Name the blood parasite species.
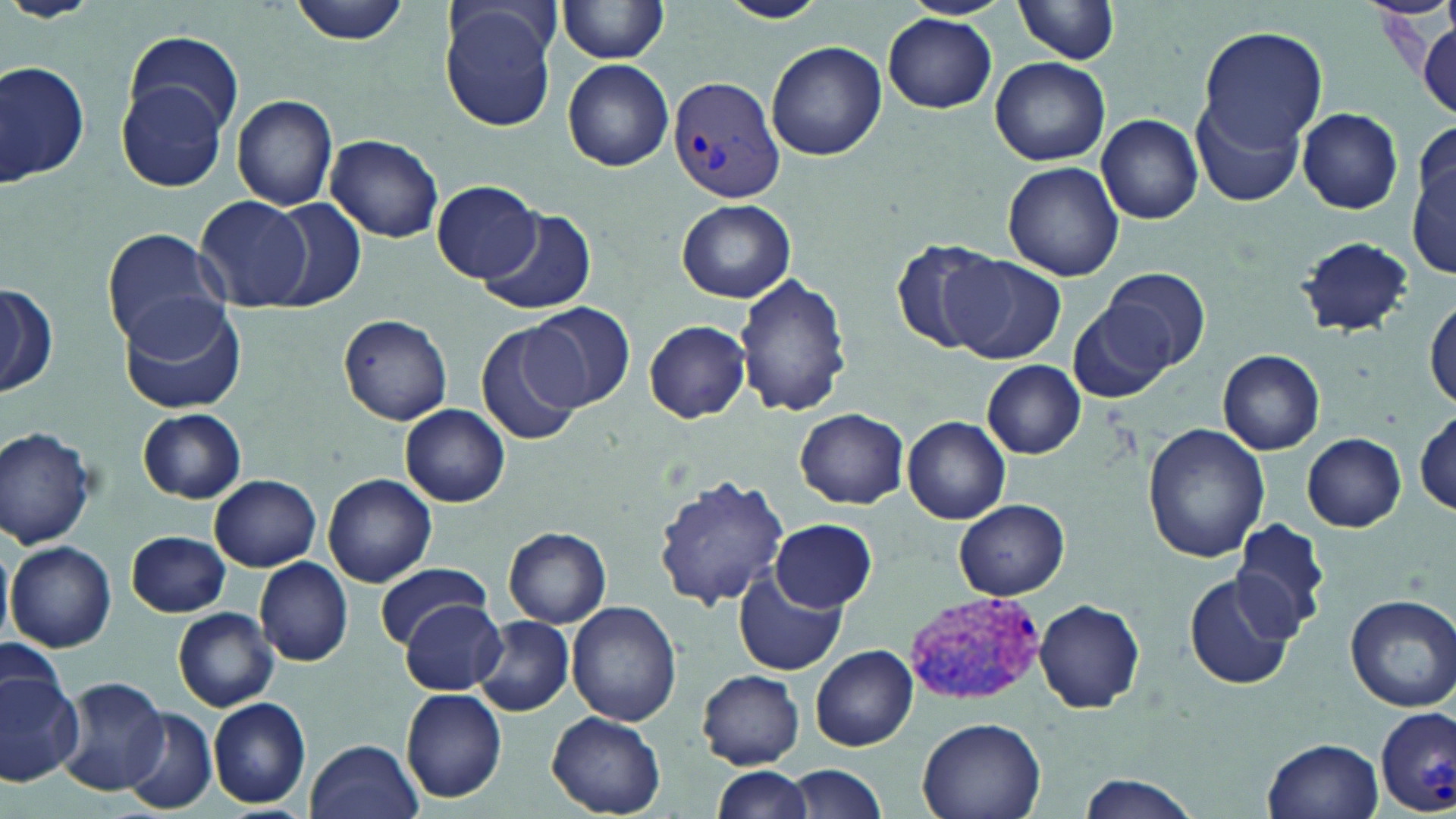

Plasmodium vivax.

magnification: 1000x
stain: May-Grünwald-Giemsa
field_of_view: one of a larger specimen
preparation: thin blood film
plasmodium_vivax_infected_red_blood_cell_locations: 'approximate bounding boxes as (x1,y1)-(x2,y2) corner pairs in pixels: (666,74)-(786,206), (901,593)-(1045,704), (1376,706)-(1456,812)'
image_size: 1456×819 pixels
modality: optical microscopy
uninfected_red_blood_cell_locations: 'approximate bounding boxes as (x1,y1)-(x2,y2) corner pairs in pixels: (288,0)-(412,44), (718,0)-(828,24), (1017,1)-(1120,64), (556,2)-(670,63), (438,3)-(559,133), (883,13)-(997,112), (1414,23)-(1455,120), (1199,27)-(1328,150), (123,32)-(245,137), (766,41)-(886,161), (991,57)-(1110,165), (1,58)-(90,188), (562,60)-(674,172), (117,81)-(227,193), (230,94)-(338,210), (1194,98)-(1305,208), (1296,108)-(1404,214), (1097,113)-(1203,224), (325,135)-(445,243), (1411,148)-(1454,277), (1002,161)-(1125,281), (432,180)-(545,283), (194,196)-(313,312), (263,198)-(365,308), (677,199)-(796,304), (478,210)-(597,315), (102,227)-(227,352), (1296,235)-(1414,337), (891,237)-(1008,354), (945,254)-(1066,365), (1099,266)-(1214,375), (734,272)-(852,418), (1,283)-(55,399), (119,294)-(250,414), (1427,297)-(1456,408), (1069,298)-(1176,403), (525,301)-(635,411), (337,314)-(454,426), (644,320)-(751,422), (475,321)-(586,447), (1218,350)-(1323,454), (983,361)-(1086,458), (398,403)-(512,507), (136,408)-(247,503), (794,408)-(908,508), (1416,410)-(1454,514), (904,416)-(1010,524), (1143,424)-(1270,561), (0,426)-(98,549), (1302,433)-(1406,531), (322,473)-(436,587), (654,474)-(791,611), (208,476)-(321,571), (954,499)-(1069,599), (1233,516)-(1334,641), (772,518)-(876,612), (504,526)-(611,628), (127,530)-(230,618), (0,540)-(14,650), (7,541)-(116,652), (255,558)-(353,667), (373,562)-(495,648), (1182,570)-(1299,691), (734,573)-(845,676), (1344,594)-(1456,712), (398,597)-(508,694), (1033,598)-(1145,713), (567,601)-(682,726), (173,607)-(279,710), (472,616)-(574,717), (0,639)-(68,720), (810,646)-(917,751), (0,670)-(83,784), (698,671)-(804,767), (56,677)-(169,796), (400,688)-(508,803), (207,698)-(312,809), (548,710)-(667,816), (122,711)-(217,813), (915,718)-(1046,819), (1262,737)-(1384,818), (305,738)-(423,819), (713,764)-(814,819), (785,764)-(889,819), (1075,774)-(1202,819)'